Assess this cell for malaria.
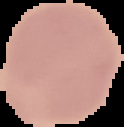
Uninfected.

Summary:
  - Image type: segmented cell region with the area outside set to black
  - Image size: 124×127 pixels
  - Preparation: thin blood film